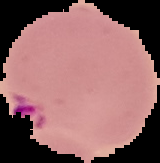
Summary:
  - Image type: segmented cell region on a black background
  - Image size: 160×163 pixels
  - Result: Plasmodium parasites identified
  - Preparation: thin blood smear